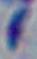 1000x magnification. Toxoplasma gondii is seen. Micrograph.